Give a bounding box for every Plasmodium parasite.
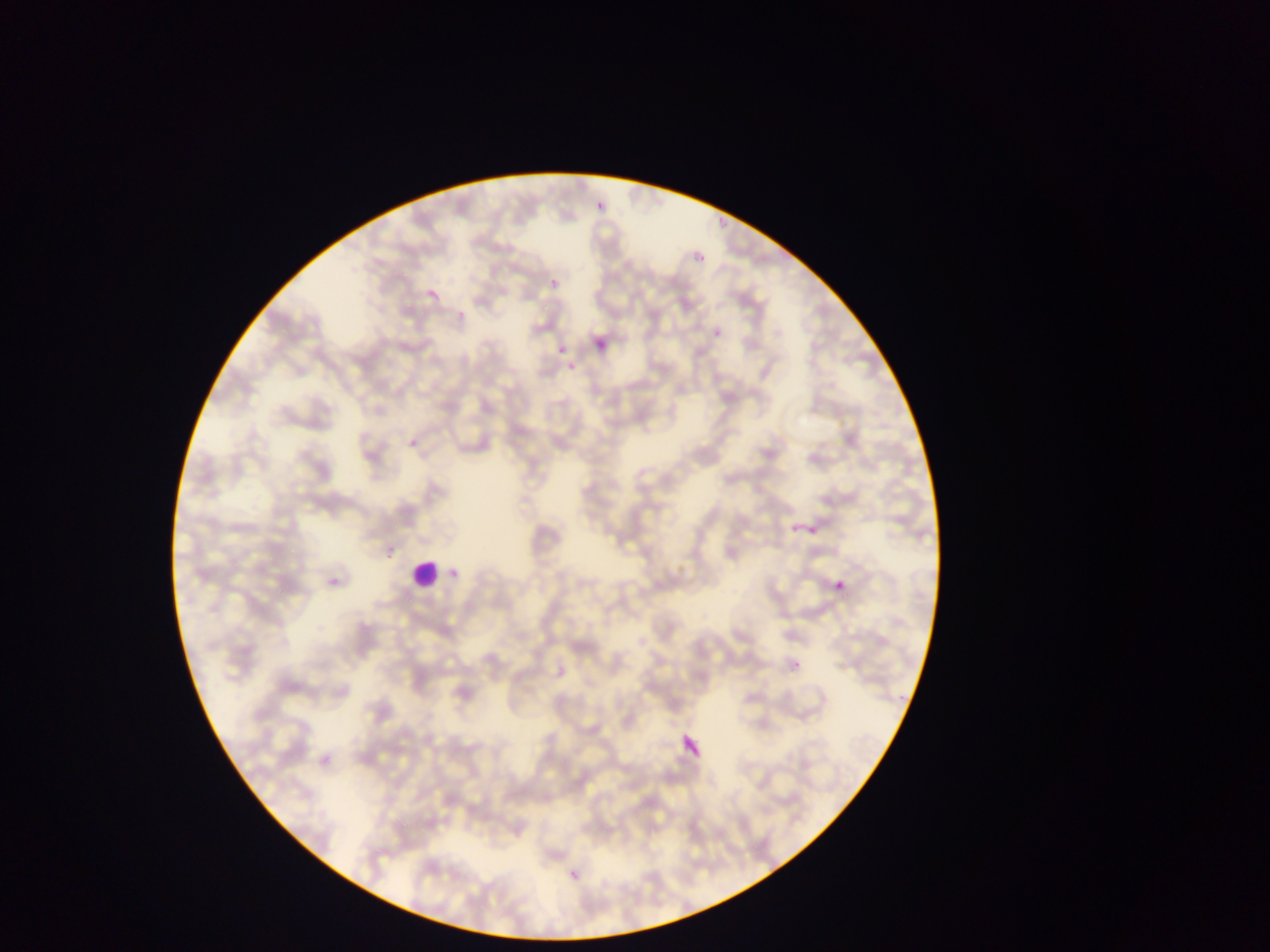

No Plasmodium parasites observed.

Approximate bounding boxes as (left, top, right, bottom) in pixels. Leukocyte locations: (412, 554, 445, 589). Thin blood film. Single field of view. Image is 1270×952 pixels. Mobile-phone photograph taken through the microscope. Collected in Ghana.